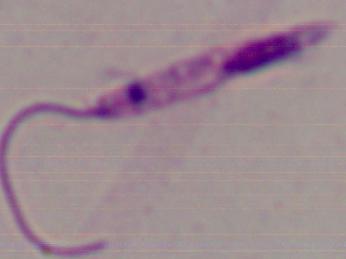

{
  "magnification": "1000x",
  "modality": "photomicrograph",
  "identification": "Leishmania"
}